Classify this cell by malaria status.
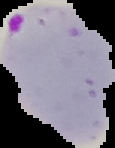

It is parasitized.

image_size: 115×148 pixels
preparation: thin blood smear
image_type: segmented cell region on a black background